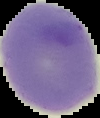
From a thin blood film. Result: negative for malaria parasites. Cell region segmented out of the field of view; the surrounding area is masked to black. Image is 100×118 pixels.